Identify the parasite.
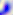
This is Toxoplasma gondii.

Captured at 400x magnification. Photomicrograph.